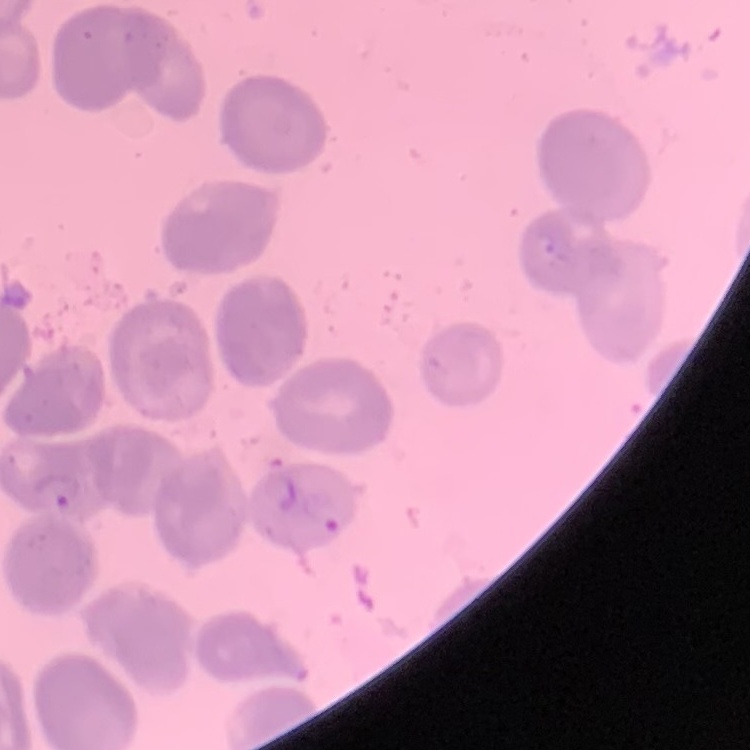
The red blood cells exhibit no rouleaux formation. Thin blood film. Stained with either Field's or Giemsa. Square crop of a larger photomicrograph.